Give a bounding box for every malaria parasite.
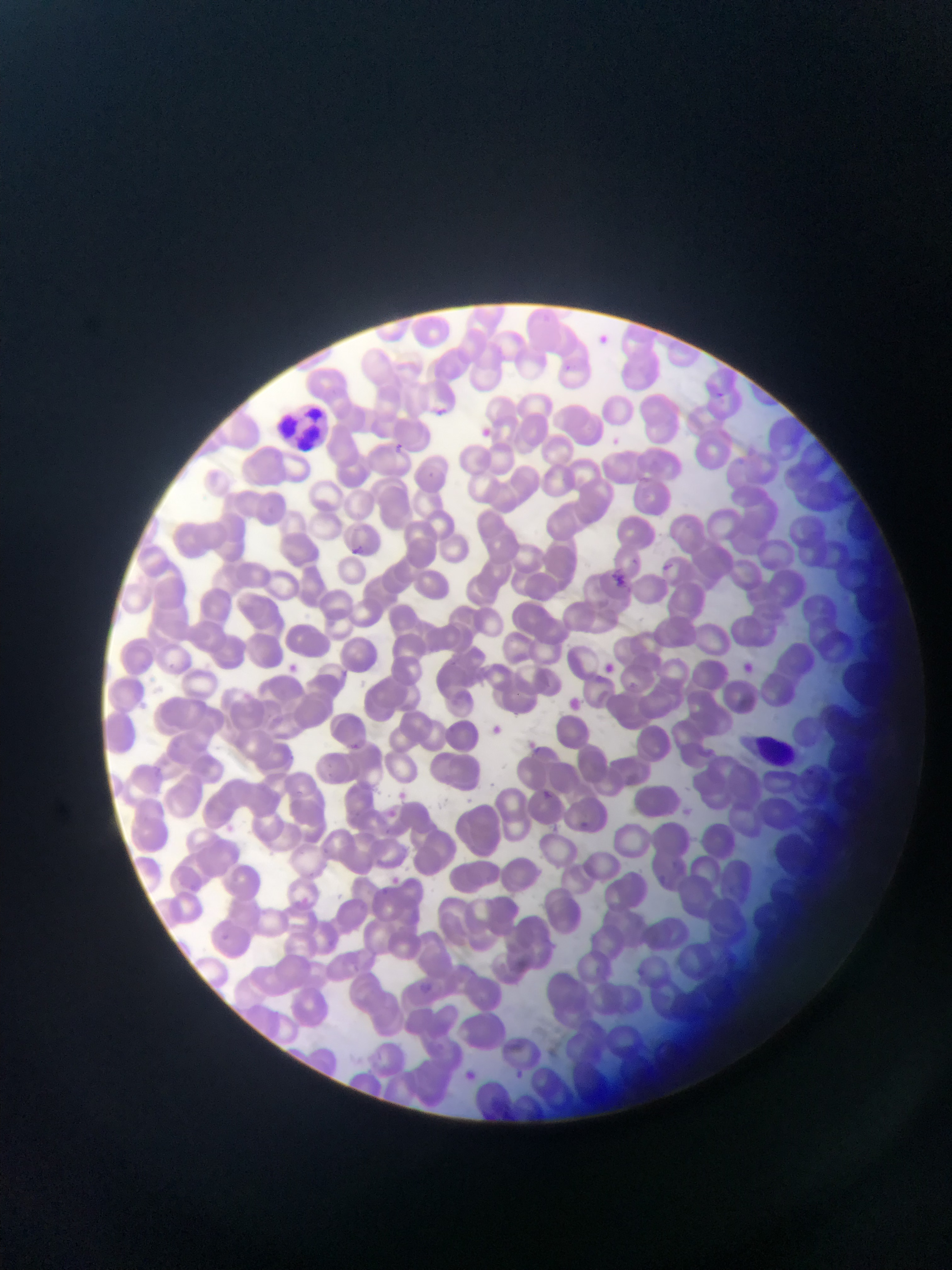
Approximate bounding boxes as {left, top, right, bottom} in pixels.
Malaria parasites: {427, 402, 450, 422}, {476, 424, 494, 441}, {391, 441, 407, 456}, {343, 544, 362, 560}, {608, 572, 629, 592}, {732, 656, 761, 682}, {281, 659, 304, 679}, {599, 660, 619, 677}, {563, 694, 585, 715}, {483, 721, 505, 740}, {347, 739, 364, 755}, {542, 784, 569, 811}, {395, 787, 412, 803}, {576, 812, 596, 842}, {386, 872, 404, 889}, {518, 955, 536, 976}, {416, 974, 431, 1000}.

Summary:
  - Leukocyte locations: {274, 397, 335, 456}, {750, 734, 800, 767}
  - Image size: 952×1270 pixels
  - Country: Ghana
  - Capture: mobile-phone photograph through a microscope
  - Field of view: single
  - Preparation: thin blood film